Name the cell type shown.
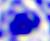
This is a leukocyte.

modality: photomicrograph
magnification: 400x